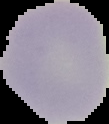

Image is 109×124 pixels. Malaria status: uninfected. The area outside the segmented cell region is set to black. From a thin blood smear.